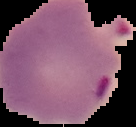
malaria status = parasitized
image size = 136×127 pixels
preparation = thin blood smear
image type = segmented cell region with the area outside set to black